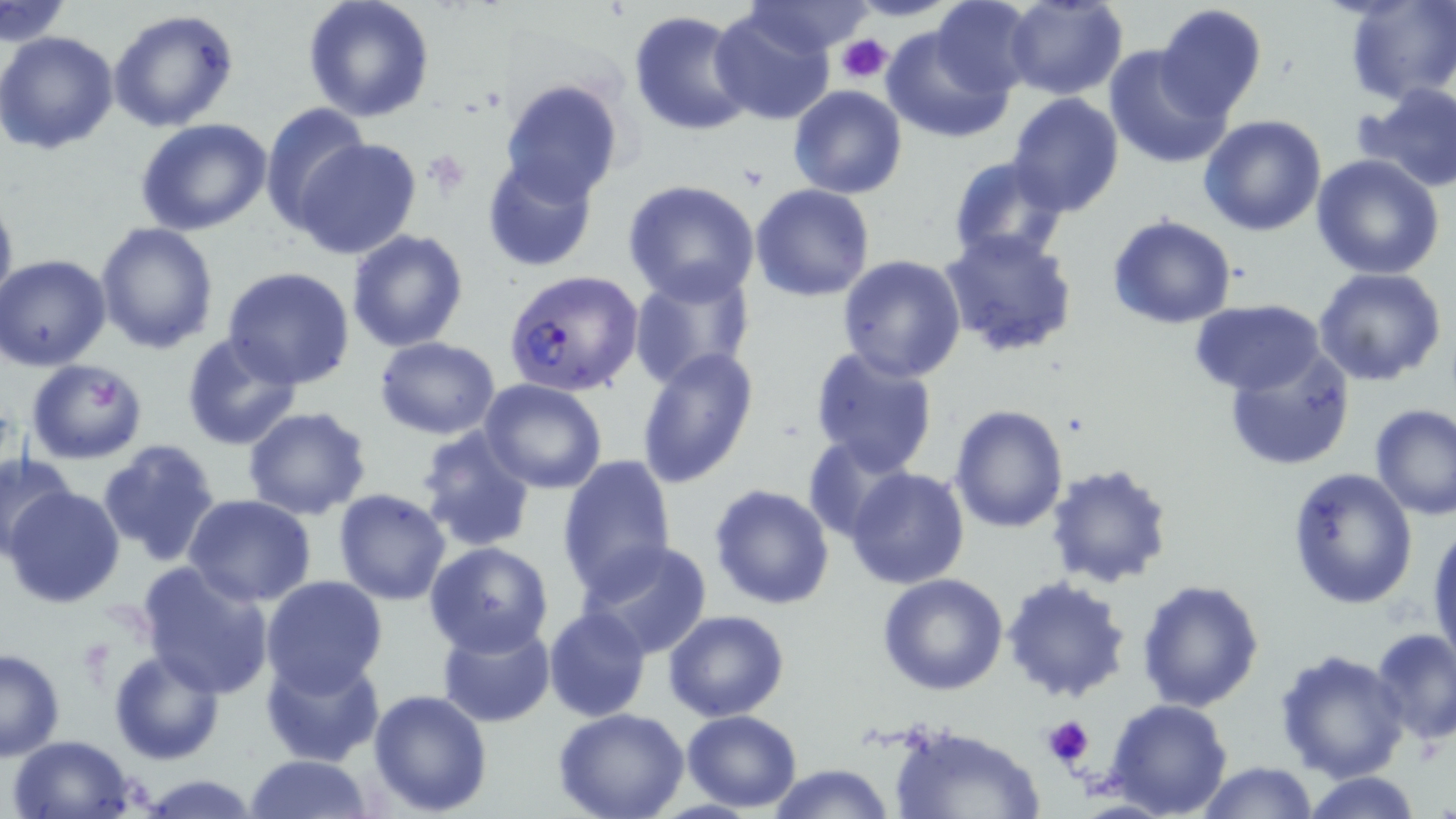
Approximate bounding boxes as (x1, y1, x2, y2) in pixels. Uninfected red blood cell locations: (302, 0, 436, 121), (1004, 0, 1127, 100), (741, 1, 879, 57), (1, 2, 71, 45), (929, 2, 1037, 96), (1342, 2, 1455, 107), (1155, 5, 1267, 123), (710, 7, 835, 124), (108, 9, 237, 132), (628, 9, 754, 136), (883, 22, 1013, 144), (0, 31, 120, 155), (1102, 46, 1231, 169), (498, 78, 624, 204), (1357, 83, 1456, 192), (788, 85, 907, 199), (1006, 92, 1125, 216), (258, 101, 372, 229), (1199, 115, 1328, 237), (134, 120, 274, 235), (293, 137, 423, 260), (1310, 155, 1445, 279), (482, 156, 599, 271), (949, 156, 1071, 266), (621, 179, 762, 303), (750, 183, 875, 301), (0, 188, 17, 314), (1107, 215, 1238, 329), (94, 223, 219, 353), (936, 228, 1079, 357), (348, 230, 467, 351), (2, 253, 113, 371), (836, 255, 968, 382), (223, 267, 355, 389), (628, 267, 755, 391), (1312, 268, 1448, 388), (1189, 298, 1326, 396), (181, 332, 303, 451), (374, 336, 502, 438), (807, 345, 939, 478), (636, 346, 760, 489), (1226, 346, 1356, 471), (23, 358, 149, 464), (478, 380, 607, 494), (1369, 402, 1456, 519), (949, 405, 1070, 533), (243, 406, 372, 520), (417, 427, 536, 551), (803, 435, 914, 544), (97, 439, 223, 566), (0, 455, 74, 554), (555, 455, 677, 599), (1045, 462, 1176, 589), (844, 467, 969, 590), (1286, 467, 1418, 608), (709, 483, 835, 609), (6, 485, 126, 608), (334, 489, 451, 605), (184, 494, 315, 607), (1429, 522, 1455, 674), (578, 540, 715, 662), (425, 542, 554, 657), (137, 561, 275, 698), (877, 573, 1008, 696), (1002, 575, 1133, 703), (259, 576, 388, 697), (1135, 579, 1266, 713), (544, 606, 652, 721), (662, 610, 790, 722), (436, 617, 557, 729), (1369, 628, 1456, 745), (394, 629, 542, 775), (1275, 647, 1408, 782), (0, 649, 66, 760), (109, 649, 227, 765), (258, 649, 385, 768), (368, 688, 493, 814), (1105, 699, 1232, 819), (553, 709, 690, 819), (681, 710, 803, 811), (889, 723, 1045, 819), (8, 735, 138, 819), (244, 753, 374, 819), (1197, 760, 1317, 818), (766, 763, 896, 819), (1300, 772, 1421, 818), (137, 774, 262, 817). Plasmodium falciparum-infected red blood cell locations: (502, 268, 642, 397). Platelet locations: (836, 34, 893, 84), (421, 152, 470, 192), (1040, 715, 1095, 773). Slide-level diagnosis: Plasmodium falciparum. Image is 1456×819 pixels. May-Grünwald-Giemsa stain. Thin blood film. Light microscopy. Captured at 1000x magnification. Single field of view.